Comment on the morphology of the erythrocytes.
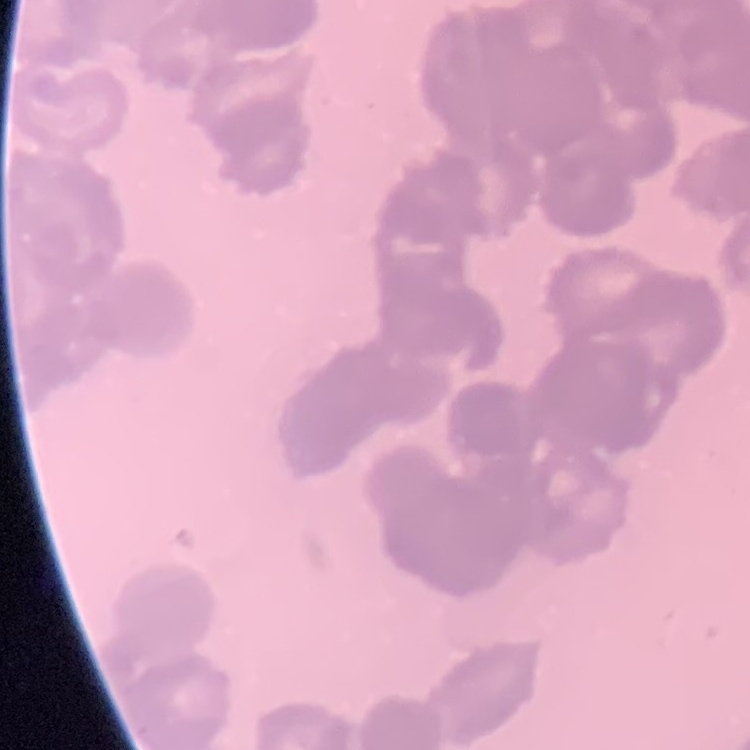

Rouleaux formation.

Summary:
  - Stain: Field's or Giemsa
  - Preparation: thin blood smear
  - Image type: square crop of a larger photomicrograph